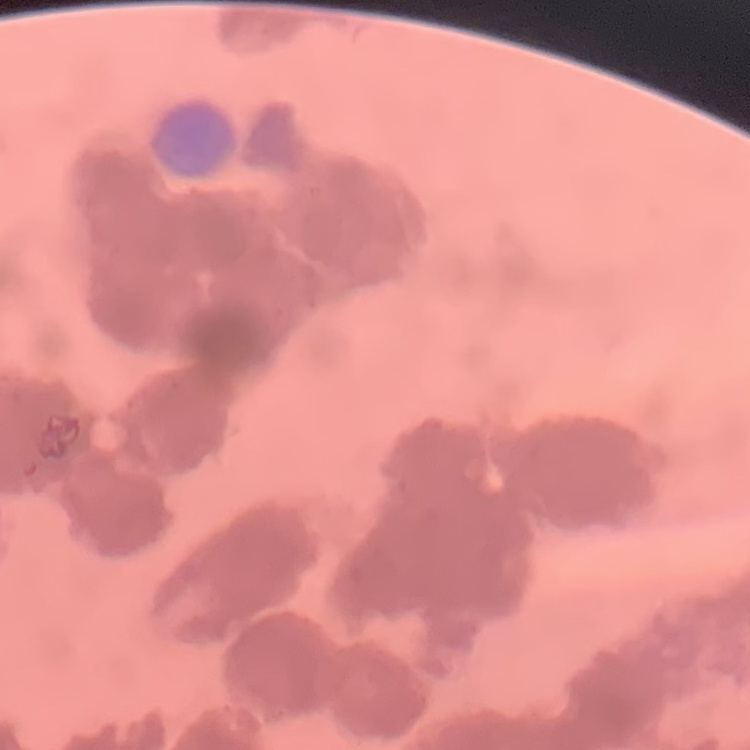
Summary:
  - Red blood cell morphology: rouleaux formation
  - Stain: Field's or Giemsa
  - Preparation: thin peripheral smear
  - Image type: square crop of a larger photomicrograph